Give the extent of all Plasmodium falciparum-infected red blood cells.
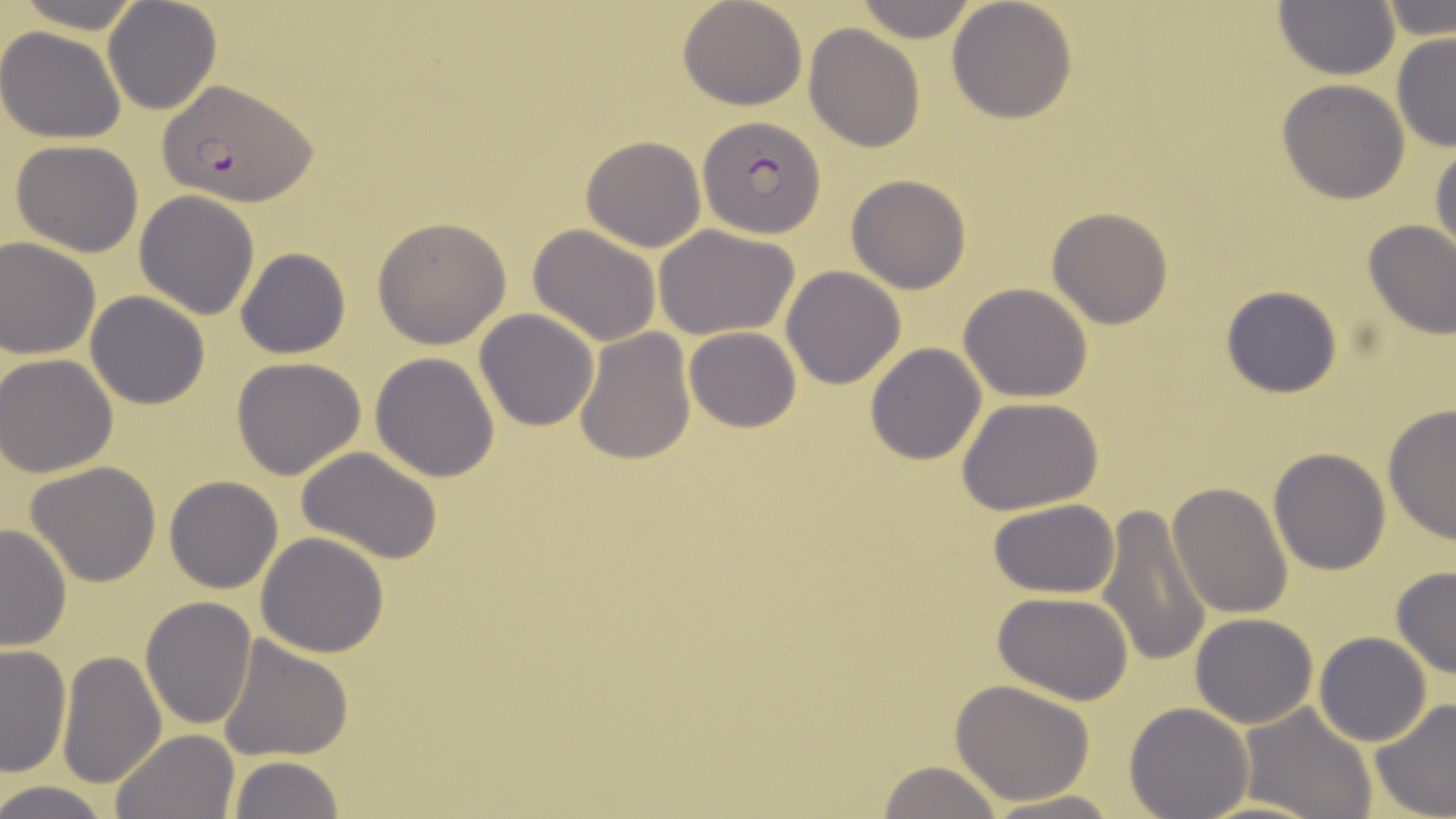

Approximate bounding boxes as [x1, y1, x2, y2] in pixels.
Plasmodium falciparum-infected red blood cells: [159, 80, 314, 206], [698, 115, 826, 238].

Summary:
  - Uninfected red blood cell locations: [7, 0, 149, 34], [102, 0, 224, 115], [679, 0, 807, 111], [947, 0, 1078, 122], [1273, 0, 1398, 80], [1378, 0, 1455, 40], [852, 1, 984, 43], [804, 24, 925, 153], [0, 26, 125, 144], [1391, 34, 1456, 154], [1277, 79, 1411, 204], [581, 135, 707, 253], [9, 139, 146, 257], [1430, 141, 1455, 262], [846, 174, 973, 294], [134, 191, 261, 319], [1046, 207, 1172, 330], [372, 217, 511, 348], [1362, 219, 1456, 340], [653, 223, 800, 341], [527, 224, 662, 348], [0, 237, 100, 359], [234, 246, 351, 359], [782, 266, 907, 389], [959, 282, 1095, 402], [1221, 284, 1344, 399], [84, 292, 210, 409], [474, 308, 599, 431], [572, 327, 696, 467], [684, 327, 801, 432], [864, 343, 987, 465], [1, 353, 120, 477], [369, 353, 501, 482], [231, 357, 368, 479], [959, 397, 1103, 515], [1382, 403, 1456, 544], [298, 446, 445, 567], [1269, 448, 1392, 576], [26, 461, 163, 587], [164, 475, 283, 593], [1168, 482, 1293, 619], [987, 500, 1122, 598], [1097, 503, 1213, 667], [0, 522, 73, 651], [256, 531, 390, 658], [1392, 567, 1456, 680], [991, 591, 1137, 707], [140, 598, 258, 730], [1191, 612, 1320, 729], [1314, 632, 1432, 746], [217, 635, 353, 762], [1, 644, 73, 778], [57, 649, 168, 790], [950, 680, 1098, 805], [1370, 698, 1456, 819], [1123, 702, 1253, 818], [1238, 703, 1380, 819], [110, 729, 240, 819], [229, 755, 346, 818], [875, 760, 1006, 818], [0, 780, 116, 819], [980, 791, 1121, 819], [1195, 796, 1325, 819]
  - Slide-level diagnosis: Plasmodium falciparum
  - Magnification: 1000x
  - Modality: optical microscopy
  - Stain: May-Grünwald-Giemsa
  - Image size: 1456×819 pixels
  - Field of view: one of a larger specimen
  - Preparation: thin blood film